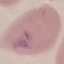
{
  "result": "no malaria parasites detected",
  "preparation": "thin blood film",
  "image_type": "automatically extracted cell patch, resized to 64 × 64 pixels",
  "capture": "smartphone camera at the microscope eyepiece",
  "stain": "Giemsa"
}